State the blood parasite species.
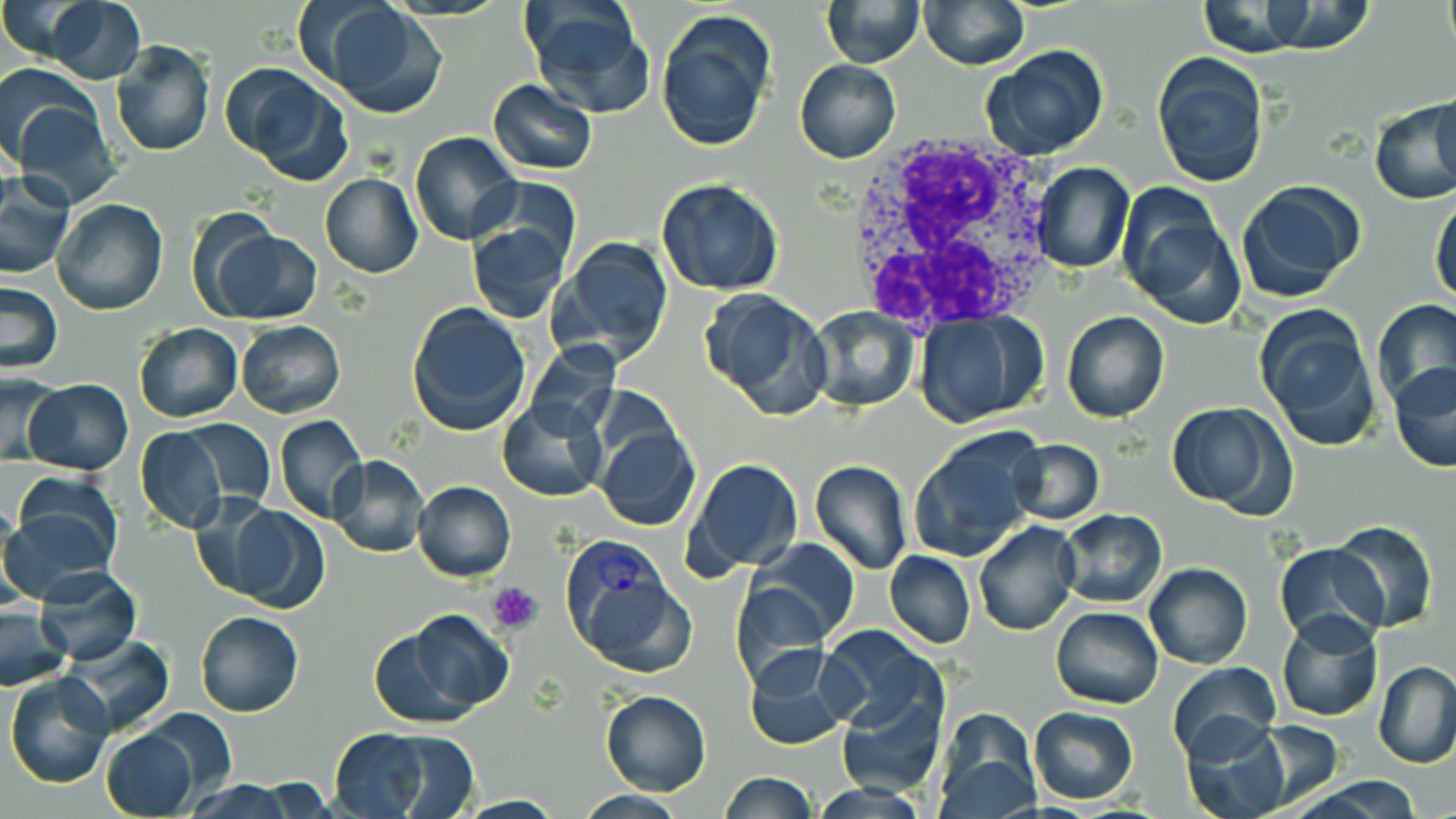
Plasmodium vivax.

stain = May-Grünwald-Giemsa
image size = 1456×819 pixels
preparation = thin blood smear
magnification = 1000x
white blood cell locations = approximate bounding boxes as (x1, y1, x2, y2) in pixels: (846, 132, 1066, 330)
uninfected red blood cell locations = approximate bounding boxes as (x1, y1, x2, y2) in pixels: (820, 0, 925, 67), (1441, 0, 1454, 57), (37, 1, 147, 84), (919, 1, 1029, 70), (312, 2, 447, 119), (524, 2, 652, 116), (1223, 3, 1377, 55), (655, 10, 775, 152), (111, 40, 216, 158), (982, 46, 1112, 162), (1150, 51, 1271, 188), (794, 59, 900, 163), (226, 62, 356, 185), (488, 79, 597, 176), (1430, 88, 1456, 194), (9, 95, 119, 205), (1369, 99, 1455, 205), (410, 131, 522, 246), (1032, 162, 1134, 273), (319, 172, 422, 278), (0, 176, 76, 280), (475, 177, 580, 268), (655, 178, 786, 296), (1234, 180, 1364, 302), (1115, 187, 1245, 331), (1430, 192, 1456, 305), (52, 199, 168, 316), (468, 220, 569, 323), (204, 228, 322, 325), (552, 236, 675, 364), (0, 281, 65, 374), (700, 288, 832, 420), (1371, 299, 1456, 408), (405, 301, 531, 436), (1253, 303, 1383, 452), (806, 306, 920, 412), (913, 309, 1050, 428), (1061, 310, 1170, 424), (235, 320, 345, 419), (133, 323, 243, 422), (526, 341, 620, 439), (1387, 359, 1456, 473), (0, 373, 62, 465), (24, 379, 132, 474), (497, 397, 608, 502), (1166, 401, 1297, 516), (276, 415, 368, 524), (181, 418, 276, 509), (594, 423, 701, 534), (134, 426, 228, 534), (909, 432, 1043, 562), (1005, 438, 1103, 524), (328, 454, 428, 558), (688, 458, 804, 574), (810, 460, 912, 576), (413, 481, 516, 582), (187, 490, 288, 596), (5, 498, 122, 602), (215, 501, 329, 612), (1058, 508, 1167, 608), (1331, 520, 1437, 633), (974, 521, 1081, 637), (746, 540, 860, 647), (1275, 541, 1387, 647), (884, 550, 976, 648), (1144, 562, 1252, 669), (33, 568, 140, 666), (732, 578, 831, 684), (1050, 607, 1163, 710), (0, 608, 71, 689), (1276, 609, 1383, 722), (195, 610, 304, 716), (370, 612, 514, 728), (817, 625, 945, 739), (60, 634, 174, 737), (744, 647, 853, 751), (1168, 660, 1281, 760), (1374, 661, 1456, 768), (5, 673, 115, 789), (601, 690, 711, 795), (837, 695, 942, 799), (1028, 706, 1140, 803), (933, 711, 1040, 817), (1179, 718, 1292, 819), (1246, 719, 1343, 808), (99, 727, 198, 818), (329, 727, 450, 817), (719, 773, 820, 818), (1290, 776, 1431, 817), (181, 780, 297, 817), (575, 790, 692, 818)
modality = optical microscopy
platelet locations = approximate bounding boxes as (x1, y1, x2, y2) in pixels: (489, 580, 544, 631)
field of view = one of a larger specimen
Plasmodium vivax-infected red blood cell locations = approximate bounding boxes as (x1, y1, x2, y2) in pixels: (562, 537, 697, 674)